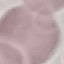

Summary:
  - Result: no malaria parasites detected
  - Image type: automatically extracted cell patch, resized to 64 × 64 pixels
  - Stain: Giemsa
  - Preparation: thin smear
  - Capture: smartphone camera at the microscope eyepiece